Locate platelets.
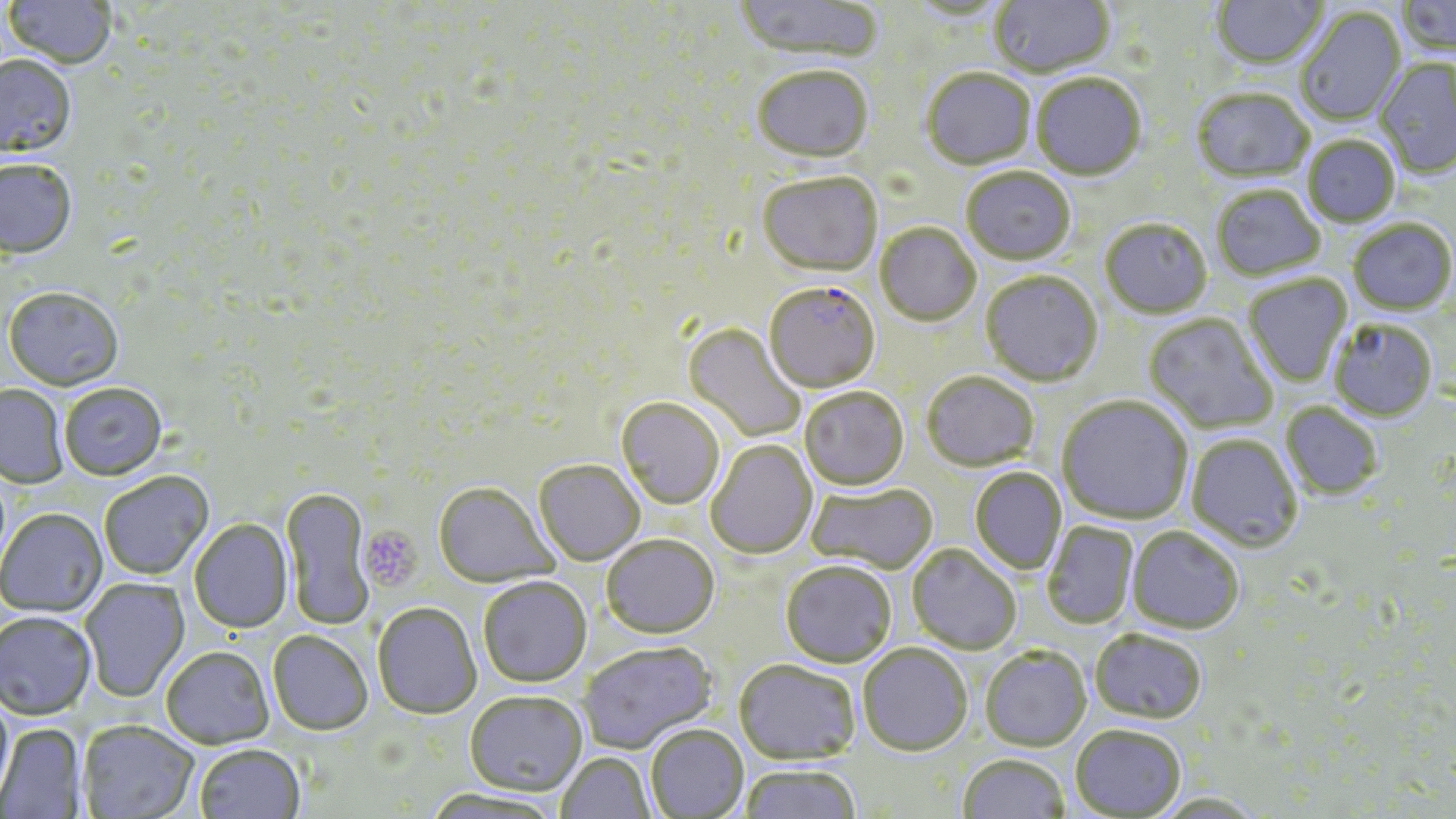

Approximate bounding boxes as (x1, y1, x2, y2) in pixels.
Platelets: (359, 526, 422, 592).

{
  "slide_level_diagnosis": "Plasmodium falciparum",
  "stain": "May-Grünwald-Giemsa",
  "preparation": "thin blood smear",
  "magnification": "1000x",
  "modality": "optical microscopy",
  "uninfected_red_blood_cell_locations": "approximate bounding boxes as (x1, y1, x2, y2) in pixels: (5, 0, 116, 72), (733, 0, 883, 64), (990, 0, 1114, 80), (1212, 0, 1329, 73), (1397, 0, 1456, 61), (904, 1, 1016, 22), (1296, 8, 1407, 127), (0, 57, 77, 162), (1374, 58, 1456, 180), (752, 69, 874, 165), (921, 70, 1036, 172), (1031, 75, 1146, 182), (1191, 90, 1314, 185), (1302, 137, 1400, 228), (0, 161, 77, 262), (961, 168, 1076, 267), (757, 174, 882, 279), (1212, 187, 1325, 282), (1348, 219, 1455, 316), (1100, 220, 1212, 320), (875, 224, 981, 328), (980, 272, 1103, 389), (1243, 275, 1353, 388), (3, 290, 124, 393), (1143, 313, 1280, 434), (1330, 319, 1439, 423), (683, 323, 806, 443), (922, 372, 1039, 472), (1, 385, 68, 489), (60, 385, 167, 482), (799, 388, 908, 491), (1056, 397, 1193, 525), (616, 398, 725, 510), (1280, 402, 1383, 500), (1186, 434, 1303, 552), (706, 440, 817, 560), (533, 461, 644, 566), (969, 467, 1067, 575), (100, 473, 214, 581), (806, 483, 936, 574), (433, 484, 558, 589), (280, 487, 374, 630), (0, 510, 107, 619), (189, 519, 293, 634), (1042, 521, 1139, 630), (1126, 527, 1244, 635), (601, 535, 719, 639), (907, 544, 1021, 655), (780, 562, 897, 668), (478, 577, 592, 690), (81, 579, 190, 703), (372, 604, 481, 721), (0, 614, 97, 722), (1089, 630, 1207, 725), (267, 632, 372, 738), (579, 643, 720, 756), (858, 643, 973, 756), (980, 647, 1092, 752), (161, 648, 274, 751), (733, 661, 860, 766), (464, 694, 587, 799), (0, 695, 15, 809), (78, 723, 199, 819), (0, 724, 86, 817), (1070, 725, 1186, 819), (646, 726, 749, 818), (195, 747, 306, 819), (556, 753, 656, 818), (957, 753, 1071, 819), (740, 765, 860, 819), (423, 791, 562, 819)",
  "image_size": "1456×819 pixels",
  "field_of_view": "single",
  "plasmodium_falciparum_infected_red_blood_cell_locations": "approximate bounding boxes as (x1, y1, x2, y2) in pixels: (765, 283, 880, 395)"
}